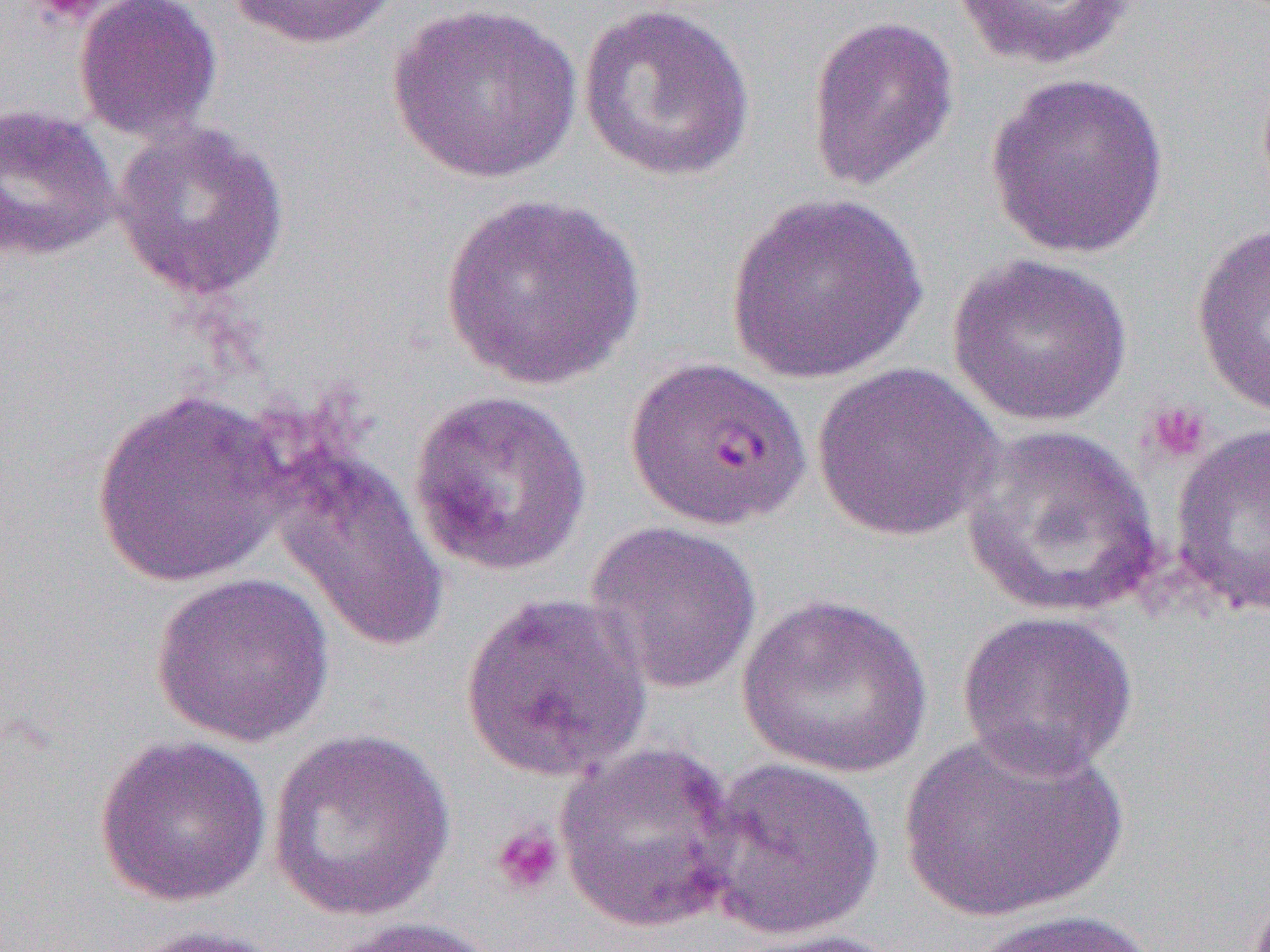

slide_level_diagnosis: Plasmodium falciparum
uninfected_red_blood_cell_locations_subset: 'approximate bounding boxes as (x1, y1, x2, y2) in pixels: (74, 0, 222, 142), (226, 0, 404, 50), (951, 0, 1137, 72), (576, 1, 757, 184), (389, 3, 581, 184), (805, 15, 960, 192), (985, 72, 1170, 260), (0, 103, 121, 263), (111, 119, 290, 302), (724, 192, 928, 385), (439, 194, 649, 390), (1190, 220, 1270, 420), (946, 252, 1132, 427), (810, 362, 1005, 543), (91, 388, 290, 587), (408, 388, 593, 578), (1168, 422, 1270, 620), (961, 423, 1164, 619), (270, 448, 449, 654), (584, 520, 763, 694), (151, 572, 335, 747), (457, 591, 654, 784), (737, 593, 932, 778), (955, 609, 1139, 780), (896, 726, 1128, 926), (266, 727, 457, 921), (93, 734, 272, 906), (554, 741, 743, 933), (699, 756, 885, 941), (965, 908, 1169, 951), (323, 916, 503, 952), (120, 922, 294, 952), (728, 927, 912, 951)'
modality: light microscopy
magnification: 1000x
platelet_locations: 'approximate bounding boxes as (x1, y1, x2, y2) in pixels: (25, 0, 111, 25), (1143, 402, 1212, 465), (490, 824, 564, 898)'
image_size: 1270×952 pixels
field_of_view: single
preparation: thin blood smear